Assess this cell for malaria.
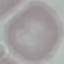

Uninfected.

preparation = thin blood smear
capture = smartphone through the microscope eyepiece
stain = Giemsa
image type = cell patch, automatically extracted from a larger field of view and resized to 64 × 64 pixels